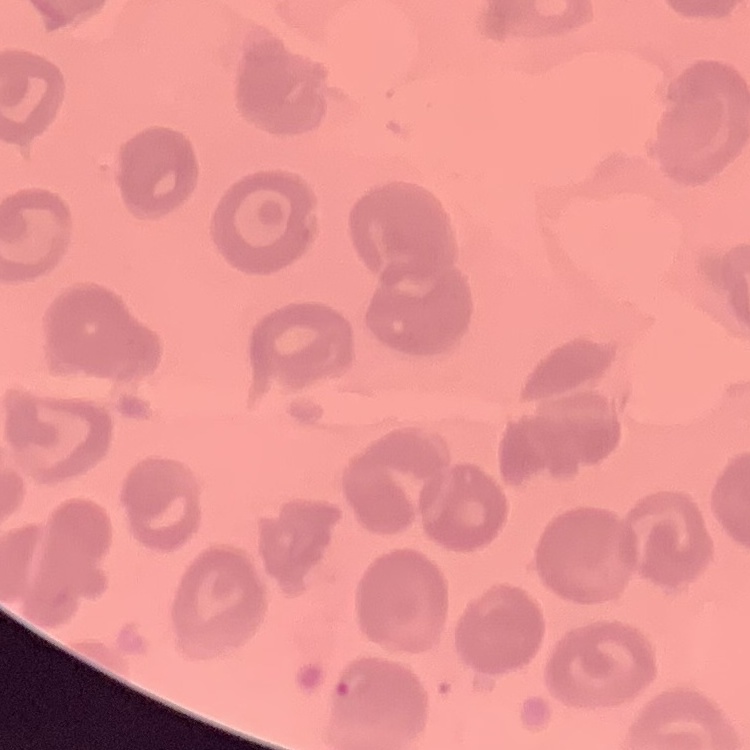 The red blood cells show no rouleaux formation. One tile cut from a larger photomicrograph. Thin blood film. Field's or Giemsa stain.